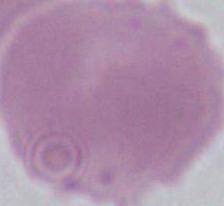
{
  "magnification": "1000x",
  "identification": "erythrocyte",
  "modality": "micrograph"
}